Comment on the morphology of the erythrocytes.
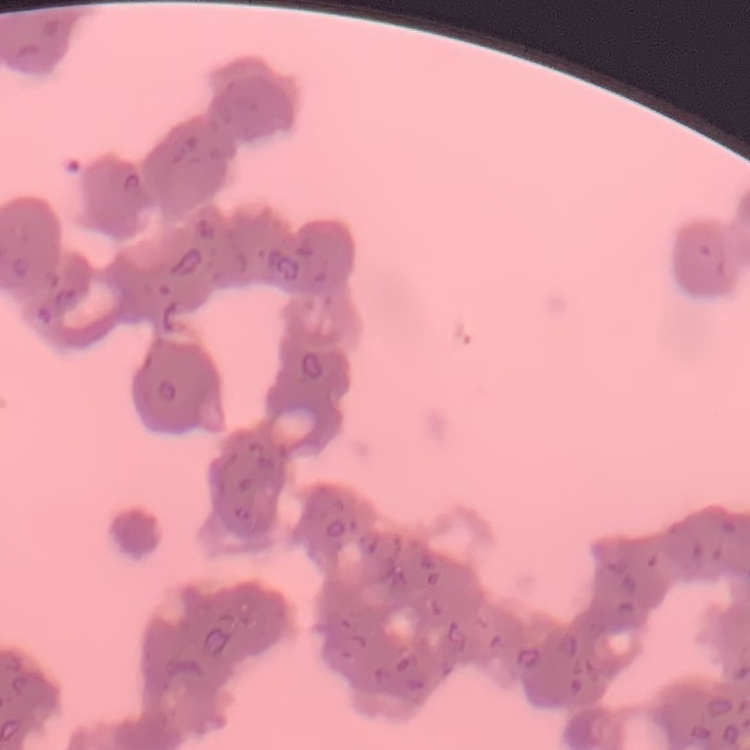
Rouleaux formation.

preparation: thin peripheral smear
image_type: square crop of a larger photomicrograph
stain: Field's or Giemsa